Locate every Plasmodium parasite.
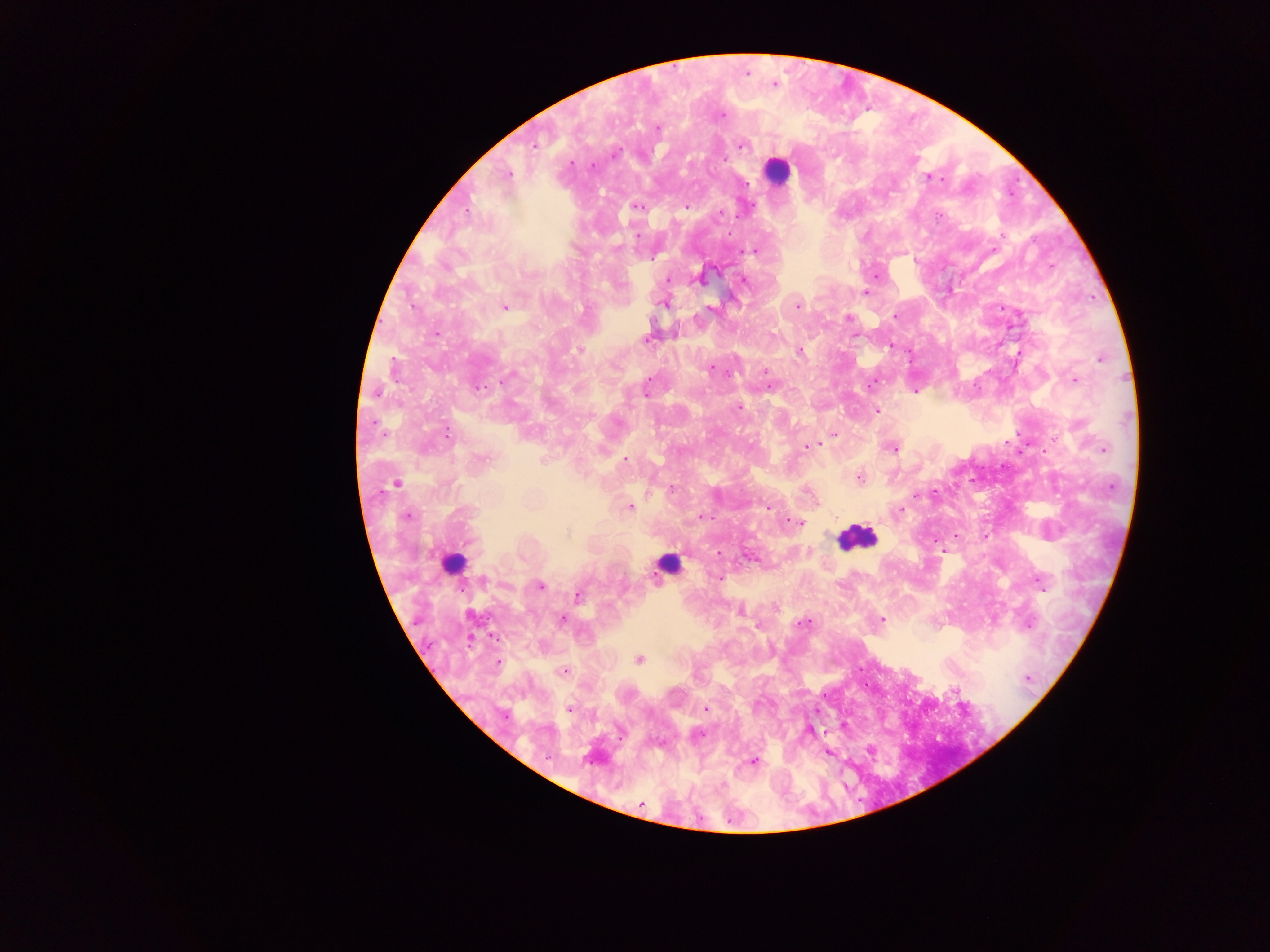

Approximate centers as x y in pixels.
Plasmodium parasites: 746 73; 774 85; 719 115; 656 128; 742 144; 533 145; 592 166; 507 175; 928 177; 635 206; 686 206; 719 213; 756 249; 877 273; 700 279; 744 280; 668 281; 866 293; 664 302; 797 304; 504 306; 711 309; 895 315; 848 318; 647 337; 579 349; 799 351; 1100 358; 710 368; 1074 379; 770 385; 915 392; 739 407; 876 410; 835 433; 1051 439; 806 447; 892 447; 1103 449; 625 458; 859 477; 396 483; 671 488; 916 495; 629 506; 900 512; 407 515; 702 517; 798 522; 956 535; 751 556; 720 577; 1039 581; 540 586; 577 595; 739 610; 561 619; 881 620; 804 623; 639 659; 496 662; 563 670; 1026 678; 954 690; 705 708; 568 709; 843 726; 698 734; 869 749; 827 752; 752 760; 641 805.

Summary:
  - Leukocyte locations: 775 170; 856 537; 453 563; 668 565
  - Image size: 1270×952 pixels
  - Preparation: thick blood smear
  - Capture: mobile-phone photograph through a microscope
  - Field of view: single
  - Country: Ghana